Assess this cell for malaria.
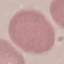

Uninfected.

Summary:
  - Image type: cell patch, automatically extracted from a larger field of view and resized to 64 × 64 pixels
  - Capture: smartphone camera at the microscope eyepiece
  - Preparation: thin blood smear
  - Stain: Giemsa